Outline each blood parasite and name the species.
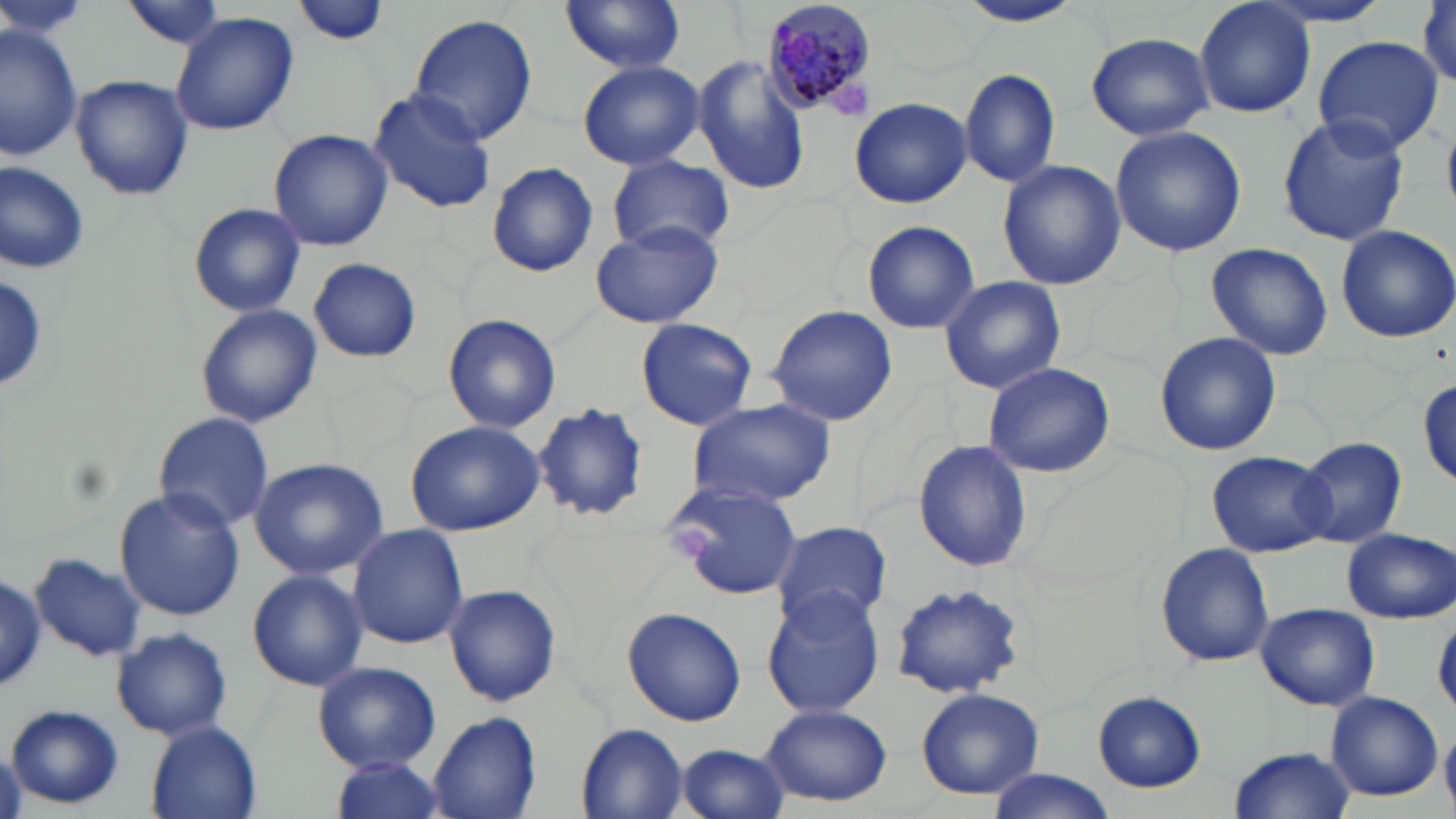
Approximate bounding boxes as [x1, y1, x2, y2] in pixels.
Plasmodium malariae-infected red blood cells: [761, 0, 881, 118].
No Plasmodium falciparum, Plasmodium ovale, Plasmodium vivax, Babesia divergens, or Trypanosoma brucei observed.

Uninfected red blood cell locations: [0, 0, 92, 42], [291, 0, 388, 48], [560, 0, 687, 75], [954, 0, 1083, 27], [1250, 0, 1400, 29], [120, 1, 228, 50], [1195, 1, 1316, 119], [170, 13, 299, 136], [407, 14, 539, 144], [1, 23, 83, 159], [1086, 32, 1215, 141], [1312, 35, 1445, 156], [694, 56, 810, 196], [577, 60, 704, 170], [958, 68, 1062, 188], [71, 75, 193, 201], [368, 89, 498, 214], [846, 97, 971, 208], [1276, 113, 1409, 246], [1110, 126, 1246, 256], [268, 130, 392, 251], [607, 155, 734, 254], [0, 159, 91, 275], [486, 160, 598, 277], [997, 160, 1127, 290], [188, 202, 307, 317], [589, 220, 726, 330], [863, 221, 980, 333], [1335, 225, 1456, 343], [1205, 243, 1335, 360], [309, 258, 422, 363], [0, 274, 48, 393], [939, 276, 1066, 394], [195, 305, 322, 427], [765, 305, 899, 427], [444, 314, 561, 433], [635, 317, 758, 430], [1155, 333, 1282, 457], [982, 360, 1114, 478], [1418, 376, 1456, 486], [684, 398, 836, 511], [532, 401, 648, 524], [153, 410, 273, 531], [404, 419, 546, 536], [1294, 435, 1407, 548], [913, 440, 1034, 573], [1209, 450, 1333, 557], [249, 457, 390, 579], [665, 478, 809, 601], [113, 487, 245, 622], [772, 519, 892, 629], [348, 523, 469, 649], [1342, 528, 1455, 622], [1155, 542, 1275, 667], [30, 550, 147, 662], [247, 569, 367, 690], [0, 574, 49, 690], [890, 582, 1025, 697], [444, 584, 562, 707], [761, 587, 885, 717], [1256, 602, 1379, 711], [623, 605, 747, 727], [112, 628, 232, 740], [312, 661, 440, 772], [914, 687, 1044, 800], [1323, 690, 1443, 802], [1092, 691, 1204, 792], [759, 702, 897, 804], [7, 705, 124, 809], [426, 710, 541, 819], [1440, 719, 1456, 811], [146, 721, 264, 819], [574, 723, 689, 819], [675, 743, 789, 819], [1229, 746, 1355, 817], [327, 756, 449, 819], [984, 770, 1114, 819]. Platelet locations: [673, 526, 717, 564]. Slide-level diagnosis: Plasmodium malariae. Thin blood film. One field of a larger specimen. Image is 1456×819 pixels. Optical microscopy. May-Grünwald-Giemsa stain. Captured at 1000x magnification.